Report the malaria status of this cell.
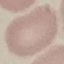

Uninfected.

{
  "capture": "smartphone through the microscope eyepiece",
  "stain": "Giemsa",
  "image_type": "cell patch, automatically extracted from a larger field of view and resized to 64 × 64 pixels",
  "preparation": "thin smear"
}